Point out each leukocyte.
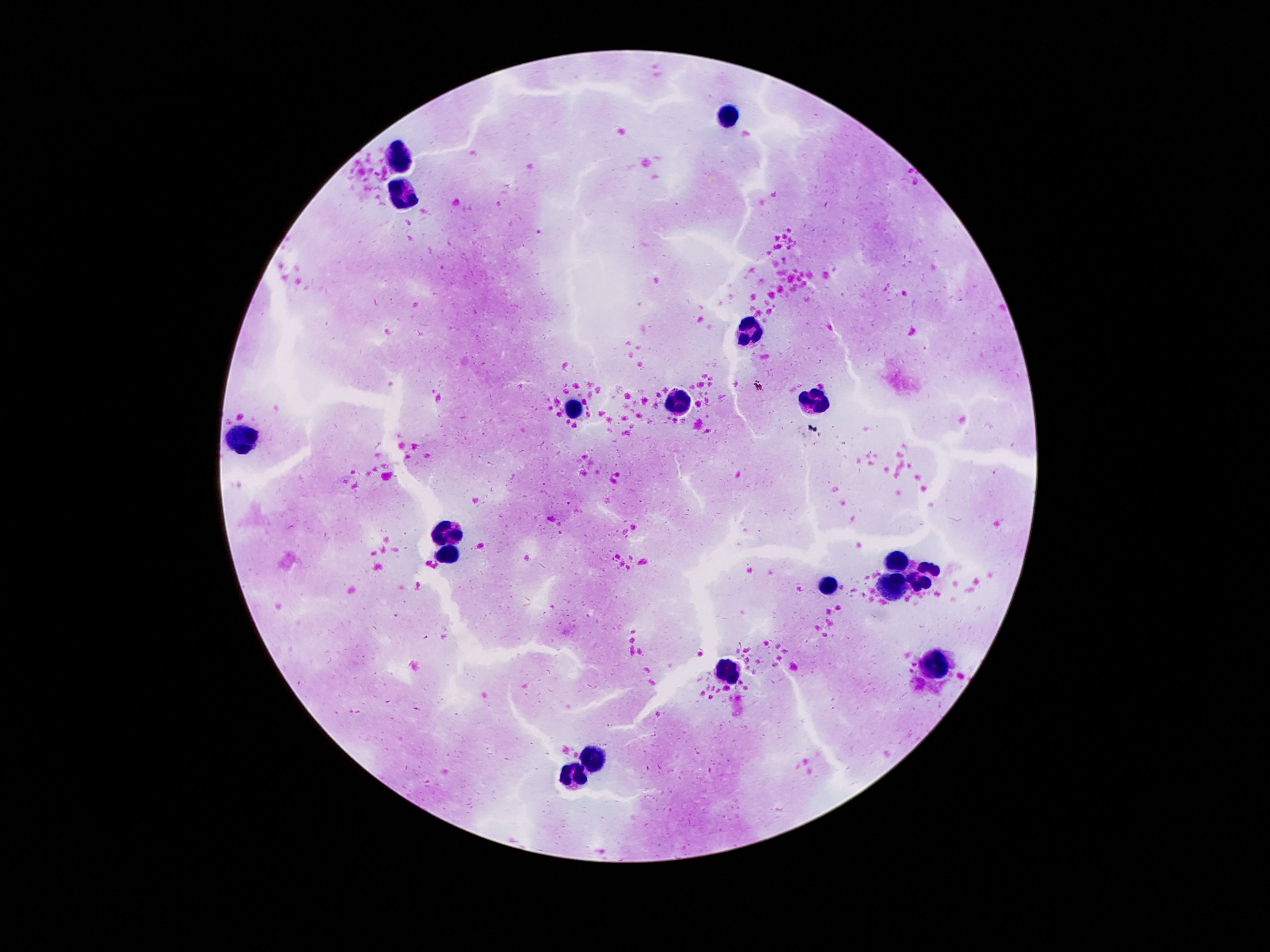
Approximate centers as [x, y] in pixels.
Leukocytes: [727, 117], [397, 161], [403, 195], [753, 332], [813, 401], [679, 404], [579, 410], [247, 433], [449, 532], [445, 556], [895, 562], [923, 576], [831, 584], [893, 588], [937, 668], [725, 670], [597, 756], [575, 776].

{
  "stain": "Giemsa",
  "field_of_view": "one from this slide",
  "magnification": "100x",
  "preparation": "thick blood film",
  "patient_malaria_status": "not infected",
  "capture": "smartphone camera through the microscope eyepiece",
  "image_size": "1270×952 pixels"
}